Assess this cell for malaria.
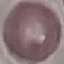
It is uninfected.

Summary:
  - Preparation: thin blood smear
  - Image type: automatically extracted cell patch, resized to 64 × 64 pixels
  - Stain: Giemsa
  - Capture: smartphone through the microscope eyepiece